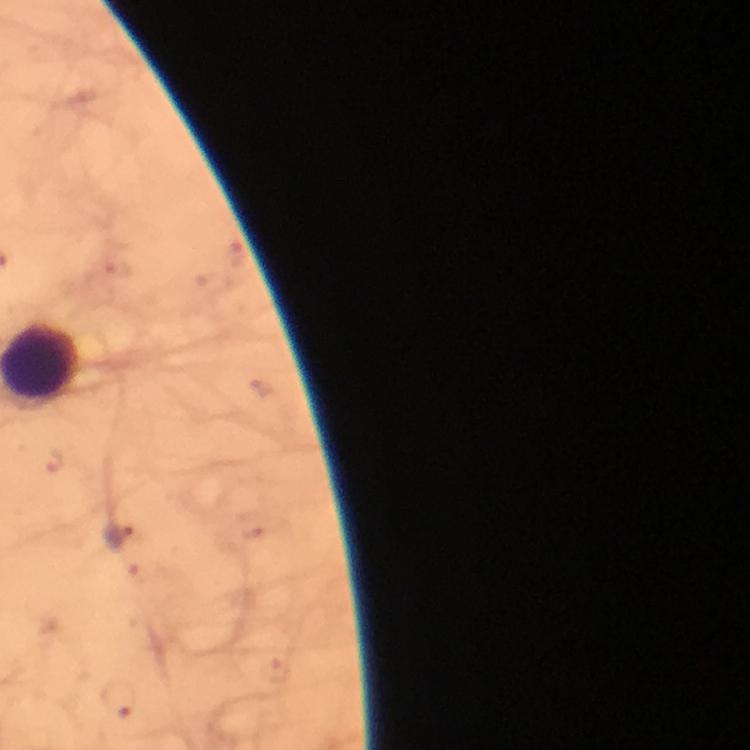
capture = smartphone photograph through a microscope
preparation = thick blood film
context = from a diagnostic examination for malaria
stain = Giemsa
magnification = 100x
image size = 750×750 pixels
immersion oil = applied
cropped from = a single field of view
malaria parasite locations = approximate object centers, in pixels from the top-left corner: (x=264, y=389), (x=54, y=463), (x=118, y=534), (x=120, y=700)